Draw a bounding box around every malaria parasite, every leukocyte, and every artifact (stain precipitate or debris).
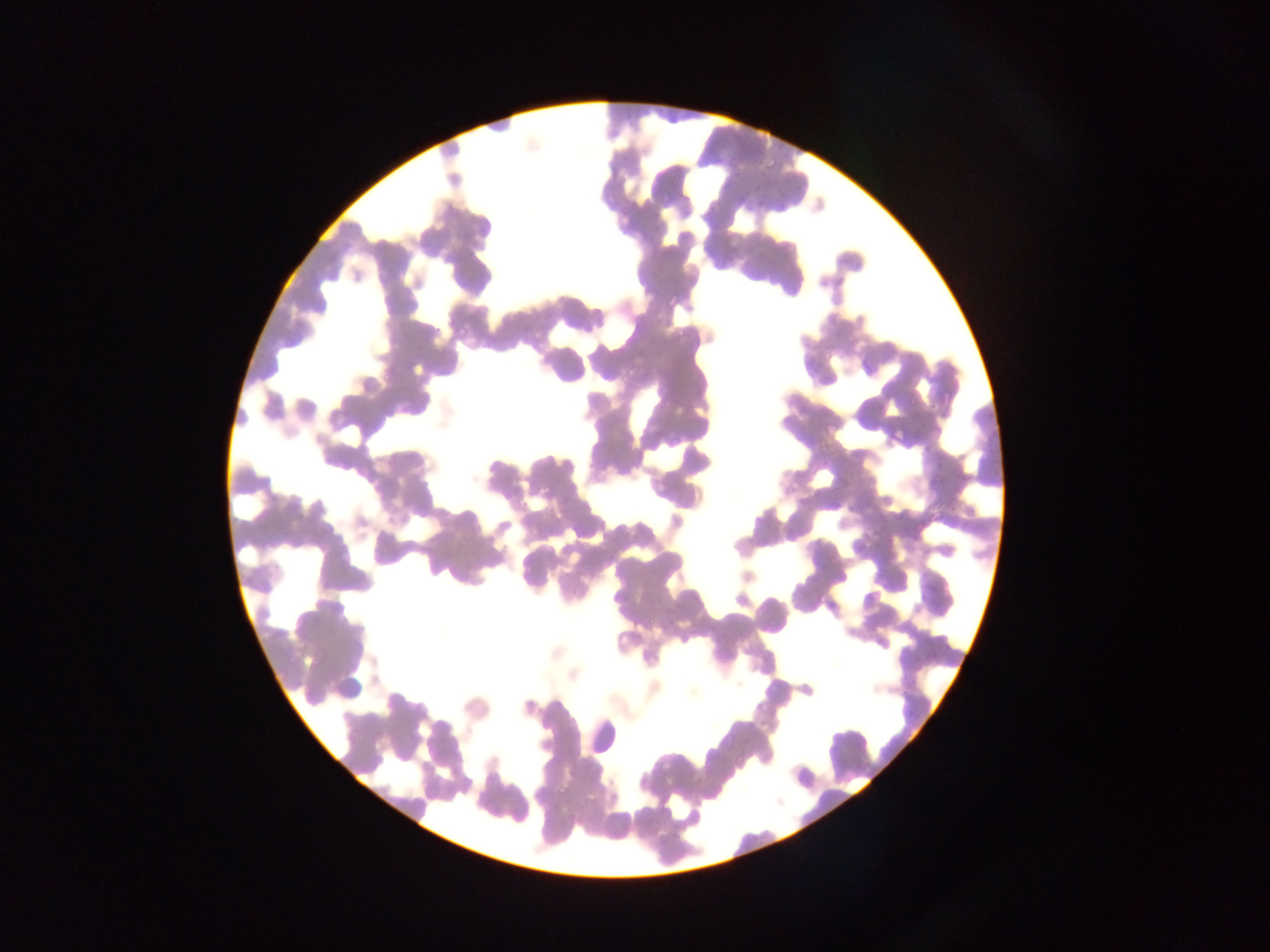
Approximate bounding boxes as [left, top, right, bottom] in pixels.
Malaria parasites: [765, 156, 780, 172], [732, 167, 739, 180], [753, 186, 761, 193], [680, 194, 691, 202], [736, 196, 746, 203], [774, 200, 789, 216], [705, 206, 713, 214], [653, 209, 661, 216], [665, 293, 680, 310], [452, 320, 469, 338], [673, 327, 691, 347], [885, 425, 905, 446], [521, 498, 529, 508], [451, 537, 467, 553], [555, 784, 570, 802] | approximate [x, y] pixel centers of objects too small to bound: [628, 116].
No leukocytes observed.

field_of_view: single
capture: mobile-phone photograph through a microscope
image_size: 1270×952 pixels
country: Ghana
preparation: thin blood smear